Name the parasite shown.
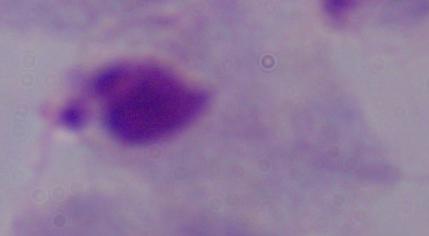

A trichomonad.

{
  "magnification": "1000x",
  "modality": "photomicrograph"
}